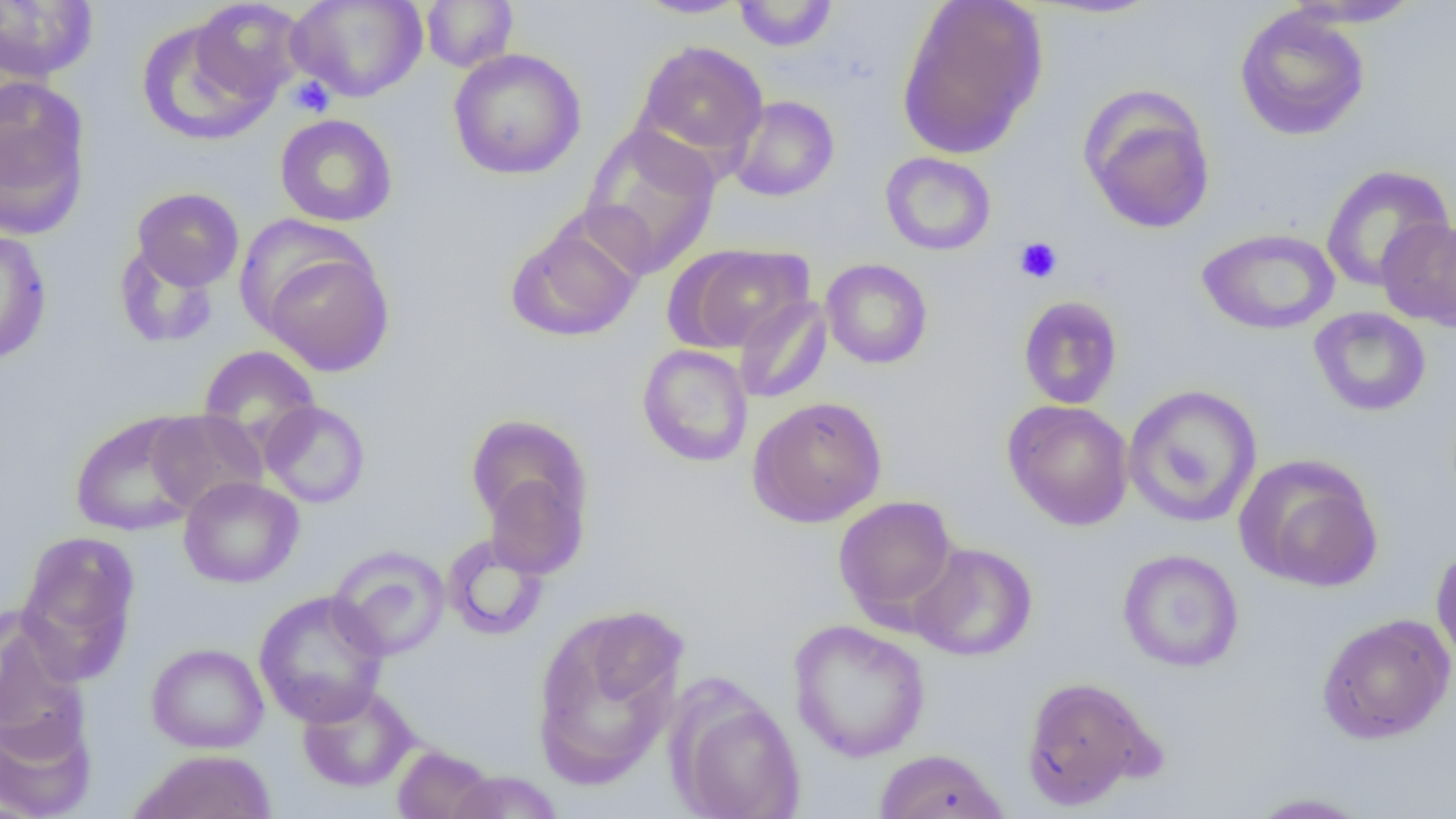
Summary:
  - Coordinate format: approximate bounding boxes as (x1,y1)-(x2,y2) corner pairs in pixels
  - Platelet locations: (288,76)-(334,117), (1014,237)-(1062,283)
  - Uninfected red blood cell locations: (189,0)-(308,104), (288,0)-(428,102), (420,0)-(518,72), (633,0)-(751,19), (895,0)-(1048,160), (0,1)-(99,82), (732,1)-(838,51), (1284,1)-(1425,28), (1234,7)-(1370,141), (135,18)-(277,145), (633,40)-(768,164), (448,48)-(586,180), (0,80)-(92,239), (1079,88)-(1216,235), (727,95)-(840,202), (274,113)-(398,227), (580,124)-(721,277), (880,151)-(996,255), (1321,164)-(1453,292), (131,187)-(244,290), (1377,217)-(1456,330), (506,218)-(644,342), (0,227)-(53,366), (1197,228)-(1340,335), (113,241)-(221,350), (674,244)-(813,353), (260,245)-(393,377), (821,258)-(933,369), (733,295)-(832,404), (1017,295)-(1124,410), (1308,307)-(1431,417), (637,344)-(754,467), (198,345)-(321,452), (1123,384)-(1262,528), (747,395)-(887,527), (1003,399)-(1134,531), (259,400)-(371,508), (145,409)-(268,514), (69,412)-(205,537), (465,414)-(591,538), (1235,454)-(1383,591), (483,470)-(590,579), (178,476)-(304,589), (832,495)-(959,625), (15,531)-(141,682), (442,533)-(549,640), (910,543)-(1038,661), (1431,544)-(1456,671), (328,545)-(450,661), (1117,548)-(1244,672), (253,590)-(390,727), (531,610)-(685,790), (1317,613)-(1455,744), (0,614)-(91,756), (788,618)-(931,762), (145,642)-(269,753), (1020,675)-(1158,809), (297,684)-(418,793), (671,688)-(805,818), (0,710)-(97,818), (391,745)-(498,819), (131,749)-(276,819), (873,749)-(1010,819), (444,770)-(565,818), (1245,791)-(1375,818)
  - Slide-level diagnosis: no evidence of blood parasites
  - Magnification: 1000x
  - Image size: 1456×819 pixels
  - Modality: light microscopy
  - Field of view: single
  - Preparation: thin blood film